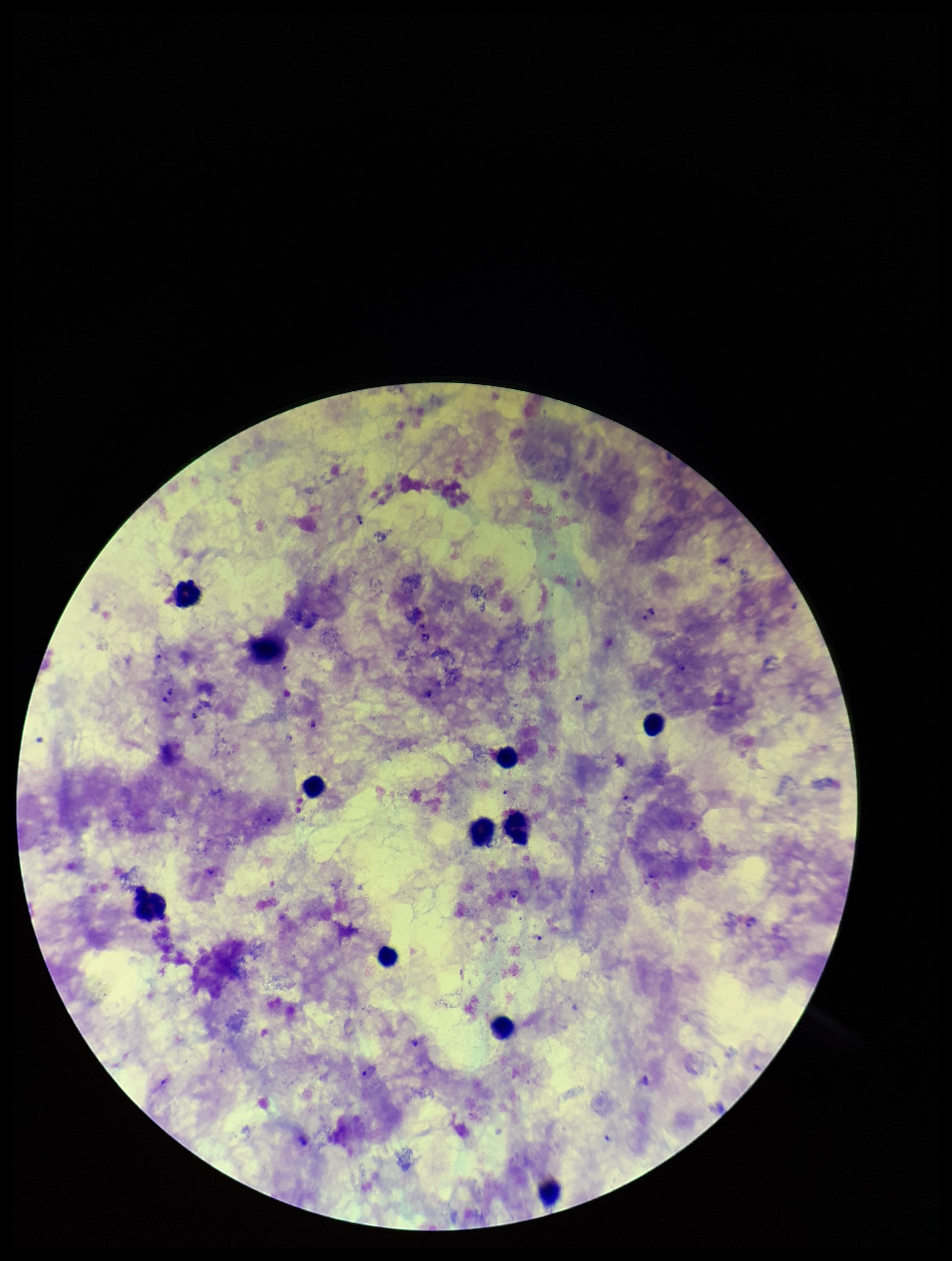
patient malaria status = infected
parasite count = 6
stain = Giemsa
field of view = one from this slide
Plasmodium parasites = detected
image size = 952×1261 pixels
capture = smartphone photograph through the microscope eyepiece
leukocyte count = 11
preparation = thick smear
species reported for this patient = Plasmodium falciparum